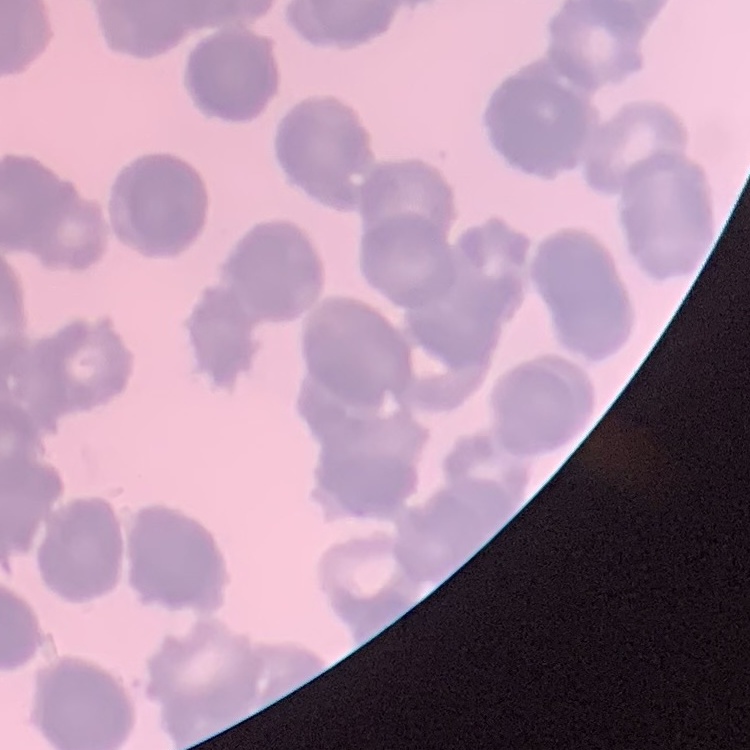
red_blood_cell_morphology: rouleaux formation
image_type: one tile cut from a larger photomicrograph
stain: Field's or Giemsa
preparation: thin blood film